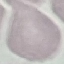
{
  "result": "no malaria parasites detected",
  "capture": "smartphone through the microscope eyepiece",
  "stain": "Giemsa",
  "image_type": "cell patch, automatically extracted from a larger field of view and resized to 64 × 64 pixels",
  "preparation": "thin smear"
}